Identify the parasite.
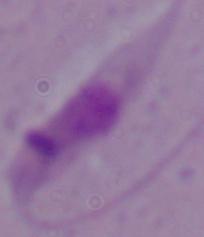

This is Leishmania.

modality = micrograph
magnification = 1000x